Locate every Plasmodium falciparum-infected red blood cell.
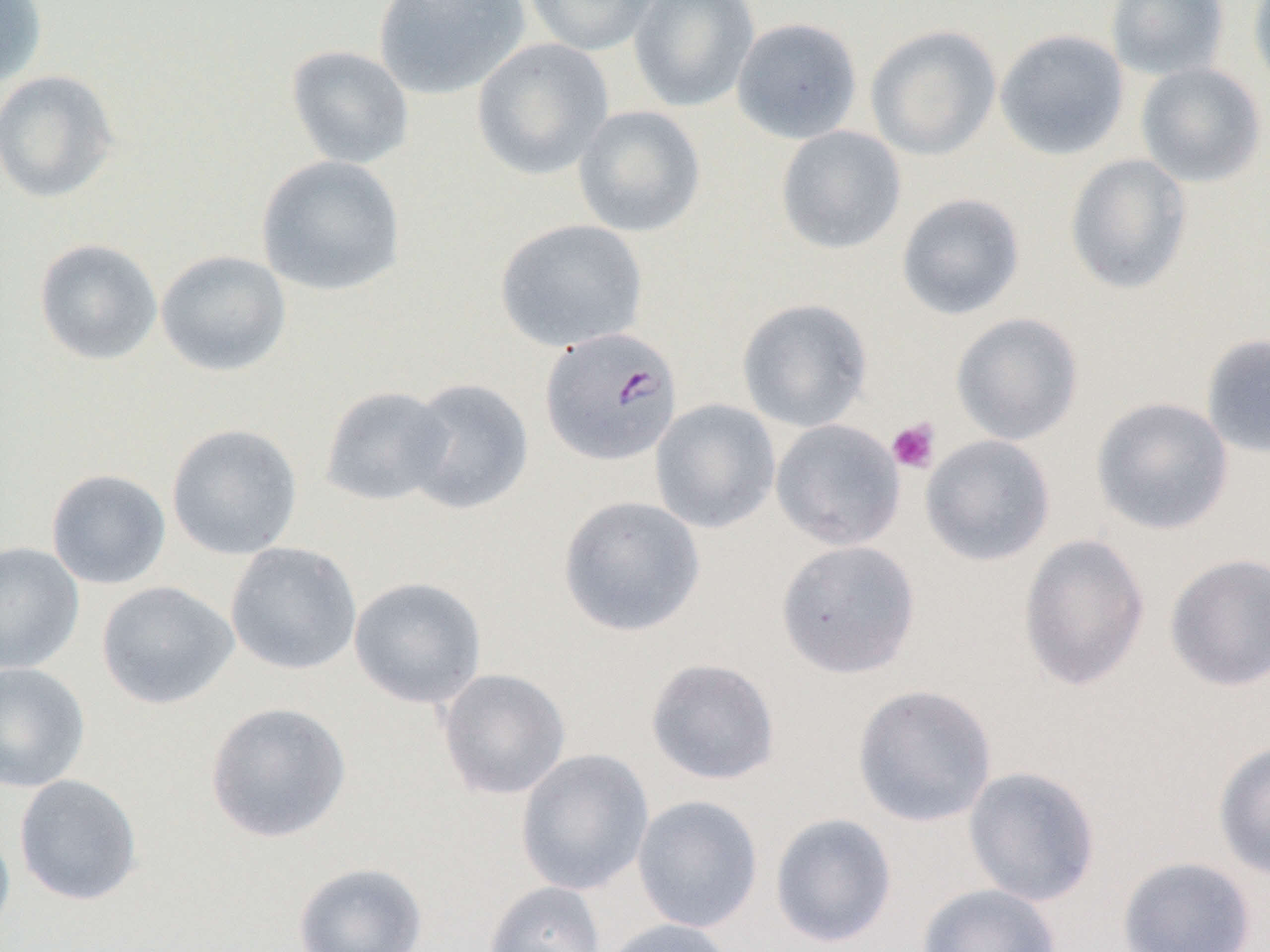

Approximate bounding boxes as [x1, y1, x2, y2] in pixels.
Plasmodium falciparum-infected red blood cells: [540, 326, 684, 467].

slide-level diagnosis = Plasmodium falciparum
image size = 1270×952 pixels
platelet locations = approximate bounding boxes as [x1, y1, x2, y2] in pixels: [886, 418, 940, 474]
uninfected red blood cell locations = approximate bounding boxes as [x1, y1, x2, y2] in pixels: [0, 0, 47, 88], [373, 0, 530, 100], [524, 0, 662, 56], [628, 0, 760, 112], [1105, 0, 1230, 82], [1248, 0, 1270, 95], [731, 17, 863, 144], [865, 24, 1001, 161], [994, 28, 1129, 161], [471, 37, 614, 180], [285, 45, 414, 169], [1135, 62, 1267, 187], [0, 70, 119, 203], [572, 105, 706, 238], [775, 125, 907, 254], [255, 154, 406, 297], [1064, 154, 1193, 295], [896, 192, 1026, 320], [495, 218, 648, 352], [34, 238, 163, 365], [155, 250, 292, 377], [736, 298, 872, 432], [950, 312, 1084, 446], [1200, 333, 1270, 460], [404, 377, 534, 515], [320, 386, 456, 507], [1091, 396, 1235, 536], [650, 398, 780, 534], [770, 419, 905, 551], [166, 423, 303, 561], [920, 434, 1055, 566], [45, 469, 171, 590], [556, 495, 706, 637], [1018, 532, 1150, 692], [775, 540, 921, 678], [0, 541, 84, 674], [225, 542, 362, 676], [1163, 552, 1270, 692], [348, 577, 487, 709], [96, 580, 239, 710], [645, 657, 781, 786], [0, 662, 90, 793], [436, 668, 571, 800], [852, 683, 998, 827], [205, 701, 352, 843], [1212, 740, 1270, 880], [514, 748, 654, 896], [962, 765, 1101, 907], [14, 774, 143, 906], [631, 795, 764, 933], [769, 813, 897, 948], [0, 820, 16, 946], [1117, 855, 1257, 951], [293, 861, 428, 952], [483, 881, 605, 952], [916, 883, 1062, 952], [598, 918, 736, 952]
modality = light microscopy
magnification = 1000x
preparation = thin blood smear
field of view = one of a larger specimen